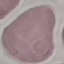
result = no malaria parasites seen
stain = Giemsa
preparation = thin smear
capture = smartphone through the microscope eyepiece
image type = automatically extracted cell patch, resized to 64 × 64 pixels